Identify the parasite.
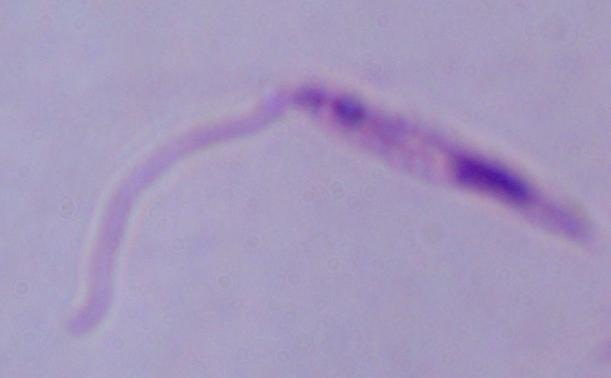
This is Leishmania.

magnification = 1000x
modality = photomicrograph